State which parasite is depicted.
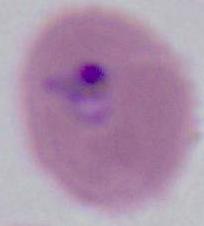

Plasmodium.

Micrograph. Captured at either 400x or 1000x magnification.